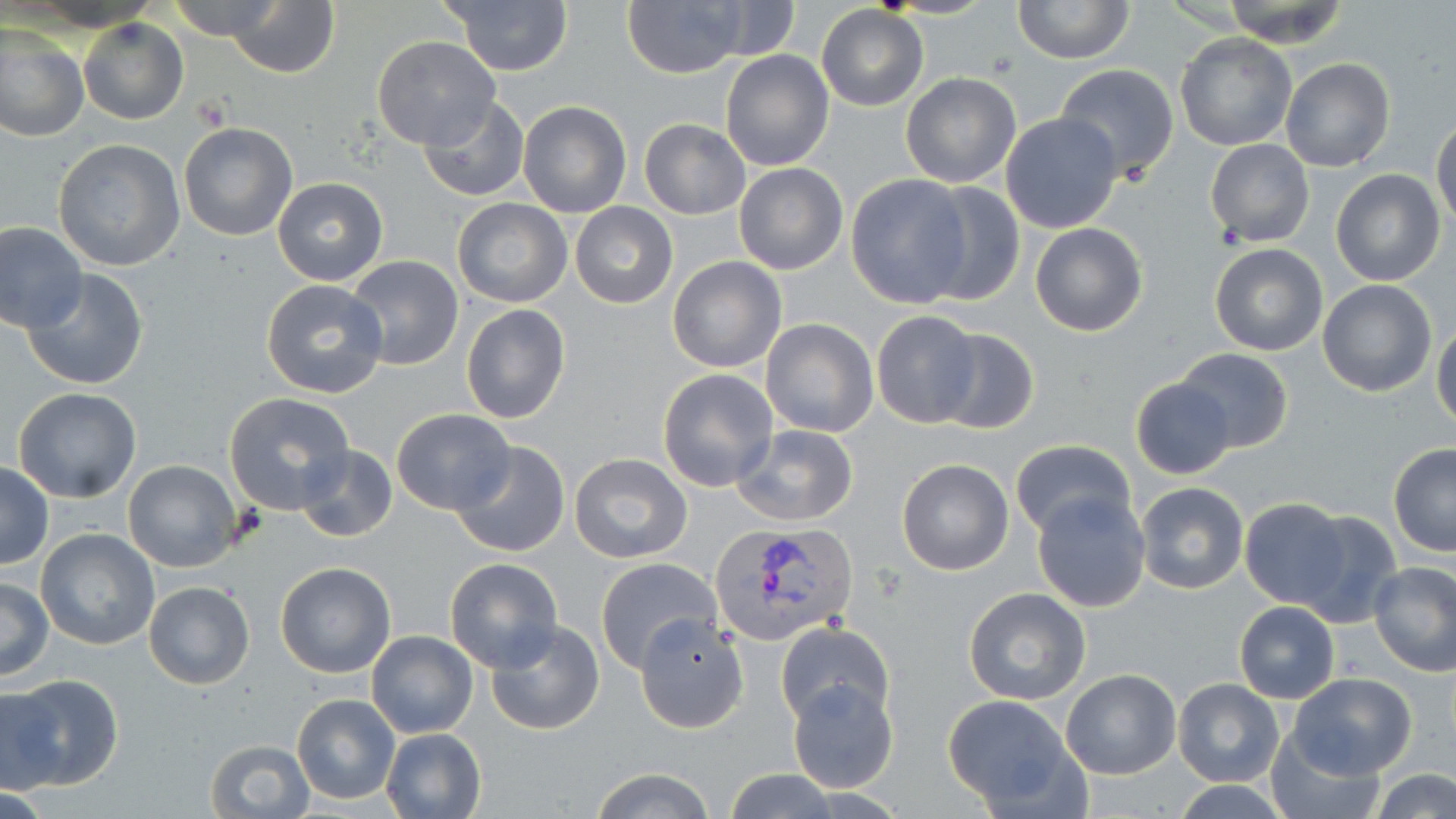

Approximate bounding boxes as named x1/y1/x2/y2 corners in pixels. Uninfected red blood cell locations: (x1=165, y1=0, x2=286, y2=42), (x1=441, y1=0, x2=573, y2=75), (x1=624, y1=0, x2=757, y2=78), (x1=1012, y1=0, x2=1133, y2=65), (x1=225, y1=1, x2=340, y2=79), (x1=1221, y1=1, x2=1350, y2=48), (x1=816, y1=5, x2=927, y2=111), (x1=79, y1=19, x2=187, y2=125), (x1=0, y1=27, x2=89, y2=142), (x1=1174, y1=33, x2=1296, y2=151), (x1=372, y1=36, x2=500, y2=151), (x1=720, y1=49, x2=835, y2=171), (x1=1280, y1=57, x2=1395, y2=173), (x1=1054, y1=64, x2=1180, y2=181), (x1=901, y1=72, x2=1020, y2=188), (x1=417, y1=96, x2=531, y2=204), (x1=518, y1=101, x2=633, y2=218), (x1=1000, y1=112, x2=1124, y2=234), (x1=1432, y1=117, x2=1456, y2=231), (x1=640, y1=119, x2=750, y2=219), (x1=179, y1=122, x2=299, y2=241), (x1=1205, y1=138, x2=1314, y2=247), (x1=53, y1=139, x2=184, y2=269), (x1=734, y1=163, x2=847, y2=275), (x1=1331, y1=168, x2=1446, y2=288), (x1=846, y1=175, x2=973, y2=309), (x1=272, y1=177, x2=388, y2=286), (x1=917, y1=182, x2=1025, y2=307), (x1=453, y1=198, x2=571, y2=308), (x1=571, y1=202, x2=678, y2=308), (x1=0, y1=221, x2=86, y2=332), (x1=1029, y1=221, x2=1148, y2=337), (x1=1208, y1=243, x2=1328, y2=356), (x1=345, y1=255, x2=464, y2=371), (x1=667, y1=256, x2=786, y2=373), (x1=20, y1=268, x2=150, y2=390), (x1=260, y1=279, x2=387, y2=400), (x1=1317, y1=279, x2=1437, y2=398), (x1=461, y1=303, x2=569, y2=424), (x1=871, y1=310, x2=982, y2=429), (x1=761, y1=318, x2=878, y2=438), (x1=1432, y1=318, x2=1456, y2=432), (x1=930, y1=326, x2=1040, y2=434), (x1=1171, y1=348, x2=1293, y2=454), (x1=658, y1=368, x2=779, y2=493), (x1=1130, y1=377, x2=1236, y2=479), (x1=12, y1=387, x2=142, y2=504), (x1=223, y1=391, x2=355, y2=515), (x1=392, y1=408, x2=516, y2=513), (x1=729, y1=424, x2=858, y2=529), (x1=1009, y1=437, x2=1135, y2=538), (x1=451, y1=440, x2=571, y2=558), (x1=292, y1=444, x2=397, y2=544), (x1=1388, y1=444, x2=1456, y2=558), (x1=568, y1=453, x2=691, y2=563), (x1=896, y1=458, x2=1015, y2=576), (x1=0, y1=460, x2=53, y2=571), (x1=122, y1=460, x2=240, y2=573), (x1=1136, y1=483, x2=1250, y2=595), (x1=1031, y1=489, x2=1152, y2=614), (x1=1239, y1=499, x2=1353, y2=609), (x1=1292, y1=509, x2=1403, y2=629), (x1=35, y1=528, x2=160, y2=650), (x1=595, y1=557, x2=720, y2=672), (x1=445, y1=558, x2=562, y2=671), (x1=1368, y1=561, x2=1456, y2=676), (x1=275, y1=562, x2=397, y2=678), (x1=0, y1=575, x2=53, y2=681), (x1=143, y1=580, x2=256, y2=689), (x1=964, y1=588, x2=1090, y2=707), (x1=1235, y1=601, x2=1340, y2=702), (x1=634, y1=614, x2=748, y2=734), (x1=485, y1=619, x2=605, y2=735), (x1=775, y1=621, x2=895, y2=726), (x1=367, y1=630, x2=478, y2=739), (x1=1061, y1=670, x2=1182, y2=778), (x1=1287, y1=672, x2=1417, y2=778), (x1=4, y1=673, x2=123, y2=790), (x1=1173, y1=678, x2=1285, y2=786), (x1=787, y1=679, x2=898, y2=794), (x1=0, y1=688, x2=64, y2=794), (x1=291, y1=693, x2=401, y2=804), (x1=943, y1=696, x2=1077, y2=809), (x1=379, y1=728, x2=487, y2=819), (x1=1266, y1=731, x2=1383, y2=818), (x1=204, y1=737, x2=316, y2=818), (x1=590, y1=766, x2=717, y2=819), (x1=723, y1=767, x2=842, y2=819), (x1=1372, y1=768, x2=1456, y2=819), (x1=1171, y1=778, x2=1290, y2=817). Platelet locations: (x1=190, y1=96, x2=231, y2=132). Plasmodium vivax-infected red blood cell locations: (x1=709, y1=522, x2=860, y2=646). Slide-level diagnosis: Plasmodium vivax. May-Grünwald-Giemsa-stained preparation. One field of a larger specimen. Thin blood film. 1000x magnification. Optical microscopy. Image is 1456×819 pixels.